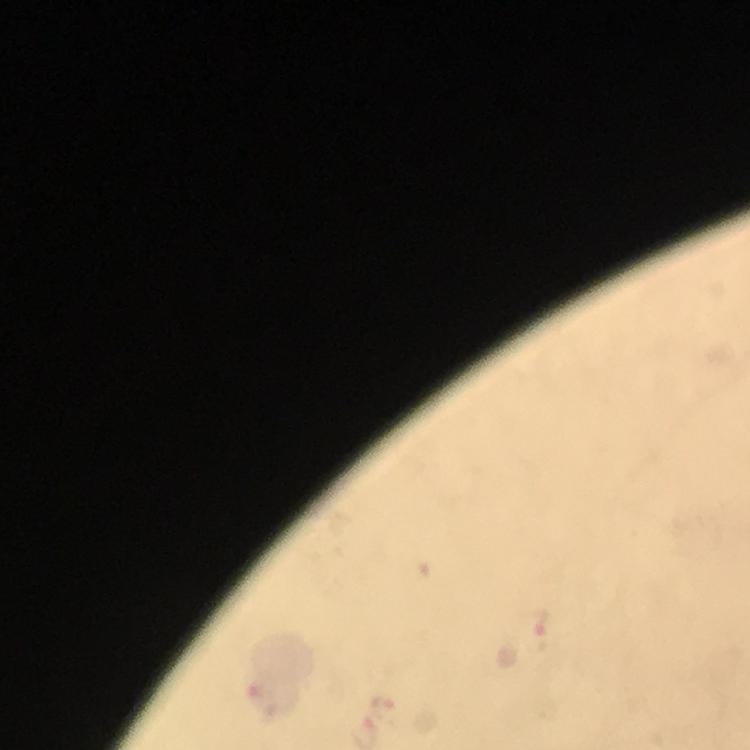
magnification = 100x
image size = 750×750 pixels
cropped from = a single field of view
capture = smartphone camera through the microscope
preparation = thick blood smear
stain = Giemsa
Plasmodium parasite locations = approximate centers as {x, y} in pixels: {538, 634}, {257, 689}, {382, 703}
immersion oil = used
context = from a diagnostic examination for malaria